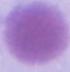
identification = erythrocyte
modality = photomicrograph
magnification = 1000x